Identify the blood parasite species.
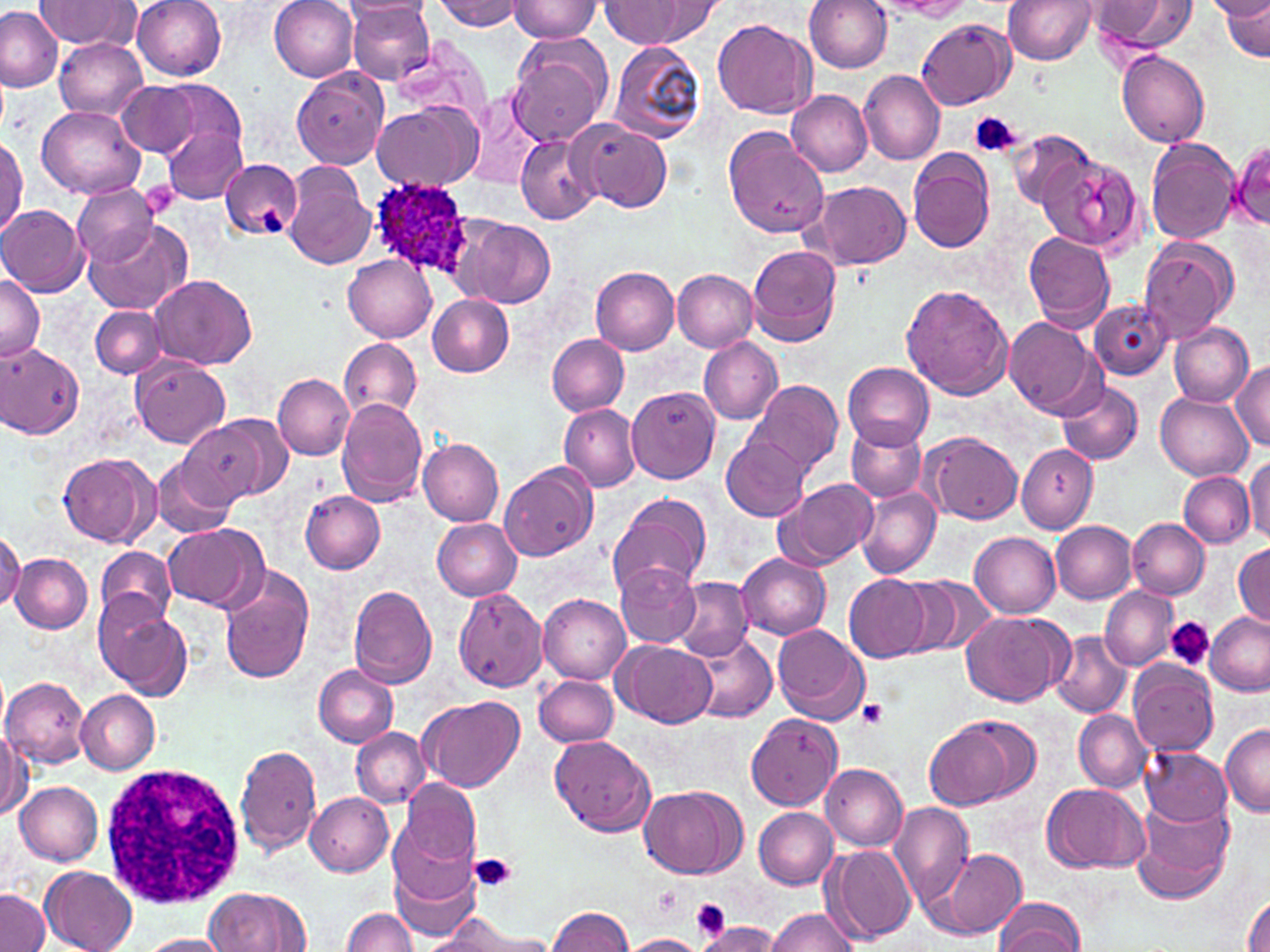

Plasmodium ovale.

stain: May-Grünwald-Giemsa
image_size: 1270×952 pixels
platelet_locations: 'approximate bounding boxes as (x1,y1)-(x2,y2) corner pairs in pixels: (970,112)-(1022,159), (142,182)-(179,219), (261,208)-(286,235), (1167,617)-(1214,672), (858,699)-(889,729), (469,853)-(519,895), (655,886)-(684,919), (691,899)-(729,937)'
field_of_view: single
plasmodium_ovale_infected_red_blood_cell_locations: 'approximate bounding boxes as (x1,y1)-(x2,y2) corner pairs in pixels: (365,179)-(478,283)'
uninfected_red_blood_cell_locations: 'approximate bounding boxes as (x1,y1)-(x2,y2) corner pairs in pixels: (34,0)-(138,48), (132,0)-(228,80), (269,0)-(360,80), (805,0)-(894,73), (885,0)-(976,18), (1092,0)-(1199,55), (1206,0)-(1270,20), (341,1)-(435,20), (347,1)-(434,84), (436,1)-(524,30), (508,1)-(601,43), (1004,1)-(1097,65), (1222,1)-(1270,60), (601,2)-(694,46), (638,2)-(726,46), (0,7)-(63,92), (711,19)-(817,119), (916,19)-(1014,108), (506,34)-(613,147), (54,38)-(148,119), (609,41)-(707,144), (1116,51)-(1209,148), (291,65)-(389,168), (858,68)-(945,166), (156,79)-(247,168), (116,81)-(199,156), (787,90)-(874,176), (461,94)-(543,192), (373,103)-(479,189), (37,105)-(144,198), (573,120)-(673,212), (721,124)-(829,241), (164,125)-(247,203), (1007,127)-(1095,209), (0,135)-(25,237), (516,136)-(600,224), (1145,138)-(1240,243), (1231,140)-(1270,229), (908,148)-(995,254), (1039,154)-(1140,251), (221,155)-(302,240), (281,162)-(375,269), (807,180)-(911,271), (71,185)-(161,266), (0,204)-(87,296), (450,216)-(554,309), (83,219)-(190,313), (1024,232)-(1116,332), (1138,237)-(1237,341), (747,244)-(842,348), (343,254)-(436,341), (591,266)-(679,355), (672,270)-(757,352), (151,273)-(257,369), (0,274)-(44,361), (900,282)-(1015,401), (427,294)-(514,378), (1089,300)-(1171,380), (90,304)-(168,378), (1004,316)-(1105,420), (1169,321)-(1253,406), (547,335)-(629,415), (698,335)-(782,424), (340,336)-(423,420), (0,343)-(85,440), (132,359)-(229,447), (1232,360)-(1270,450), (842,362)-(935,452), (273,374)-(354,461), (746,378)-(844,478), (1056,380)-(1144,467), (627,386)-(720,484), (1154,393)-(1254,481), (335,397)-(428,507), (558,403)-(641,492), (181,415)-(286,503), (846,424)-(926,502), (920,431)-(1023,524), (722,436)-(811,521), (418,438)-(504,526), (1017,443)-(1097,534), (57,451)-(157,546), (153,456)-(239,541), (1245,456)-(1270,543), (500,462)-(597,562), (1180,472)-(1255,548), (775,477)-(879,570), (855,488)-(939,578), (301,491)-(386,574), (606,491)-(712,600), (433,518)-(521,601), (1129,518)-(1209,600), (1051,520)-(1136,603), (161,523)-(266,610), (1,530)-(23,610), (970,532)-(1061,617), (1233,543)-(1270,628), (95,545)-(177,627), (9,552)-(93,633), (736,553)-(832,639), (616,565)-(702,646), (218,573)-(313,683), (844,574)-(931,663), (894,574)-(997,658), (671,578)-(752,657), (348,584)-(437,687), (1100,586)-(1177,669), (452,588)-(540,690), (538,593)-(631,684), (99,599)-(192,696), (960,610)-(1072,707), (1206,614)-(1270,696), (773,623)-(870,725), (685,630)-(776,723), (1051,631)-(1133,718), (616,640)-(715,728), (1129,660)-(1218,756), (312,664)-(400,747), (534,674)-(618,747), (0,676)-(90,768), (76,690)-(160,773), (420,694)-(523,791), (1074,710)-(1151,792), (746,714)-(842,810), (924,715)-(1029,811), (0,722)-(28,820), (1221,725)-(1270,815), (351,727)-(429,808), (551,735)-(655,836), (235,743)-(322,857), (1141,748)-(1231,827), (819,762)-(907,850), (398,778)-(480,873), (15,781)-(103,866), (1042,784)-(1149,874), (638,785)-(745,879), (304,793)-(394,877), (1133,795)-(1235,904), (887,803)-(974,913), (754,807)-(838,890), (391,813)-(480,905), (825,845)-(914,943), (938,848)-(1026,938), (391,859)-(482,943), (40,866)-(137,952), (205,888)-(313,952), (0,890)-(48,952), (1243,890)-(1270,952), (994,897)-(1086,952), (548,907)-(636,952), (767,907)-(861,952), (341,908)-(417,952), (430,913)-(551,951), (695,922)-(782,952), (137,934)-(233,951), (621,934)-(704,951)'
magnification: 1000x
modality: optical microscopy
preparation: thin blood film
white_blood_cell_locations: 'approximate bounding boxes as (x1,y1)-(x2,y2) corner pairs in pixels: (100,758)-(248,911)'